Report the malaria status of this cell.
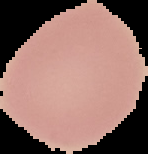

Uninfected.

Cell region segmented out of the field of view; the surrounding area is masked to black. From a thin blood smear. Image is 148×154 pixels.